Point out each Plasmodium parasite.
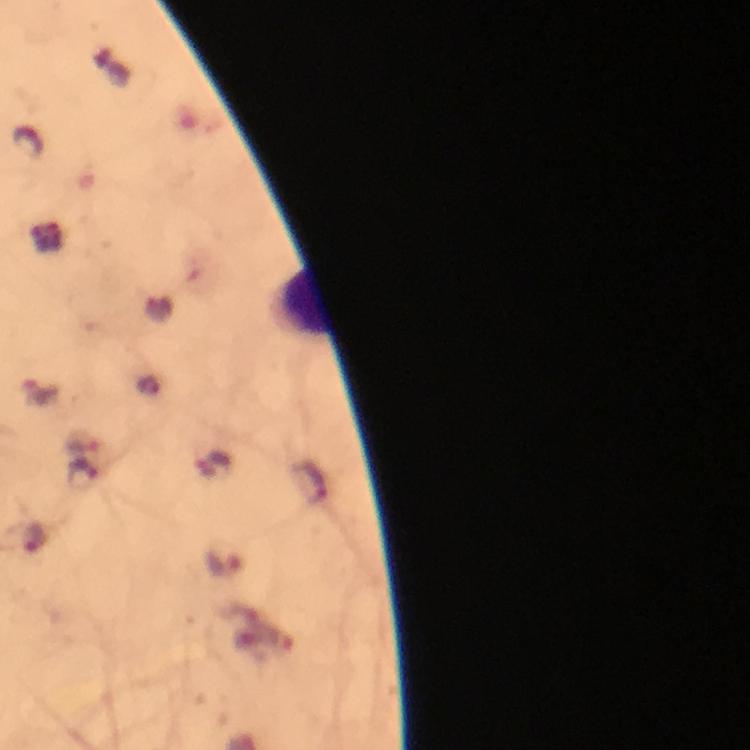

Approximate object centers, in pixels from the top-left corner.
Plasmodium parasites: (x=222, y=562).

{
  "cropped_from": "one field of view",
  "magnification": "100x",
  "context": "from a malaria diagnostic workup",
  "stain": "Giemsa",
  "immersion_oil": "used",
  "preparation": "thick blood smear",
  "image_size": "750×750 pixels",
  "capture": "smartphone mounted on the microscope"
}